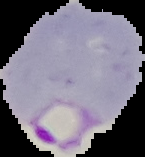

Summary:
  - Preparation: thin blood smear
  - Image type: cell region segmented out of the field of view; surrounding area masked to black
  - Image size: 145×157 pixels
  - Malaria status: parasitized